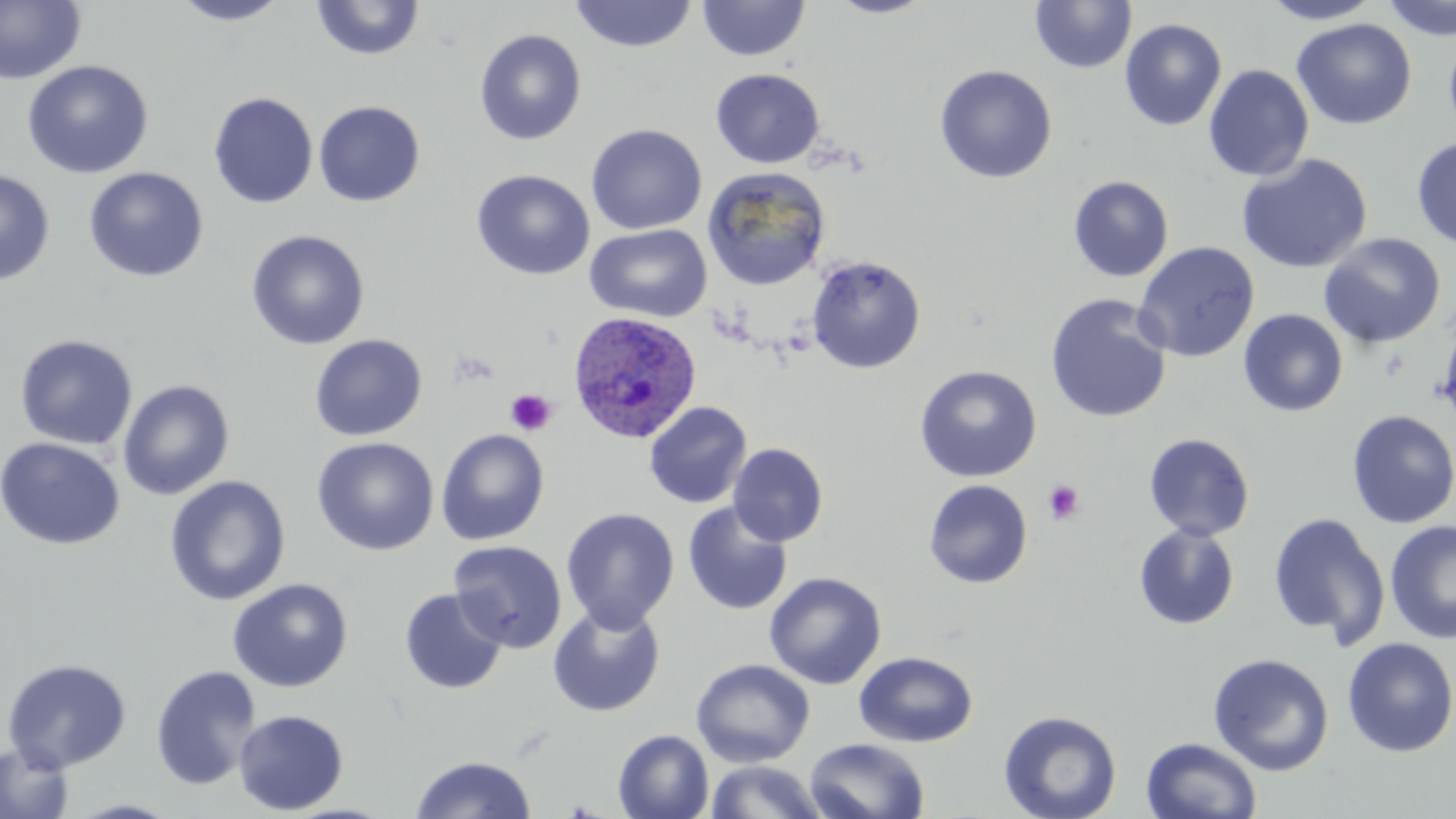 Approximate bounding boxes as [x1, y1, x2, y2] in pixels. Uninfected red blood cell locations: [0, 0, 87, 85], [171, 0, 292, 25], [310, 0, 425, 60], [826, 0, 938, 18], [1029, 0, 1137, 74], [1260, 0, 1382, 24], [1382, 0, 1456, 41], [568, 1, 698, 53], [696, 1, 810, 61], [1119, 18, 1227, 131], [1291, 18, 1417, 130], [474, 28, 587, 146], [1443, 30, 1456, 143], [21, 60, 154, 179], [934, 64, 1058, 184], [1203, 64, 1315, 182], [711, 68, 825, 168], [208, 92, 318, 209], [313, 100, 425, 207], [586, 124, 707, 235], [1411, 136, 1456, 250], [1236, 153, 1373, 274], [83, 166, 208, 282], [702, 167, 830, 291], [0, 169, 55, 286], [471, 169, 595, 280], [1068, 175, 1174, 282], [584, 224, 712, 323], [246, 229, 370, 350], [1318, 233, 1446, 349], [1133, 241, 1260, 362], [805, 255, 926, 373], [1045, 294, 1171, 424], [1238, 308, 1348, 416], [1437, 309, 1456, 424], [14, 334, 138, 451], [309, 334, 428, 441], [914, 365, 1042, 482], [117, 379, 235, 500], [644, 401, 752, 509], [1345, 410, 1456, 528], [436, 428, 550, 545], [1144, 433, 1255, 541], [0, 437, 126, 551], [311, 437, 439, 556], [728, 443, 828, 547], [164, 475, 291, 606], [923, 479, 1033, 588], [682, 502, 794, 616], [561, 507, 679, 632], [1267, 511, 1390, 649], [1384, 519, 1456, 645], [1133, 524, 1240, 630], [448, 539, 568, 653], [764, 571, 886, 689], [227, 578, 353, 692], [399, 588, 507, 695], [547, 604, 666, 716], [1341, 637, 1456, 757], [854, 651, 978, 748], [1208, 653, 1334, 776], [1, 657, 133, 773], [691, 658, 815, 768], [150, 664, 261, 790], [233, 709, 349, 815], [998, 710, 1123, 819], [613, 729, 714, 818], [1141, 736, 1263, 818], [804, 738, 930, 819], [0, 741, 75, 819], [411, 755, 536, 818], [704, 760, 828, 819], [65, 798, 183, 818]. Platelet locations: [504, 388, 557, 436], [1043, 479, 1085, 526]. Plasmodium ovale-infected red blood cell locations: [567, 310, 702, 443]. Slide-level diagnosis: Plasmodium ovale. Thin blood film. May-Grünwald-Giemsa-stained preparation. One field of a larger specimen. Light microscopy. Image is 1456×819 pixels. Captured at 1000x magnification.